State the blood parasite species.
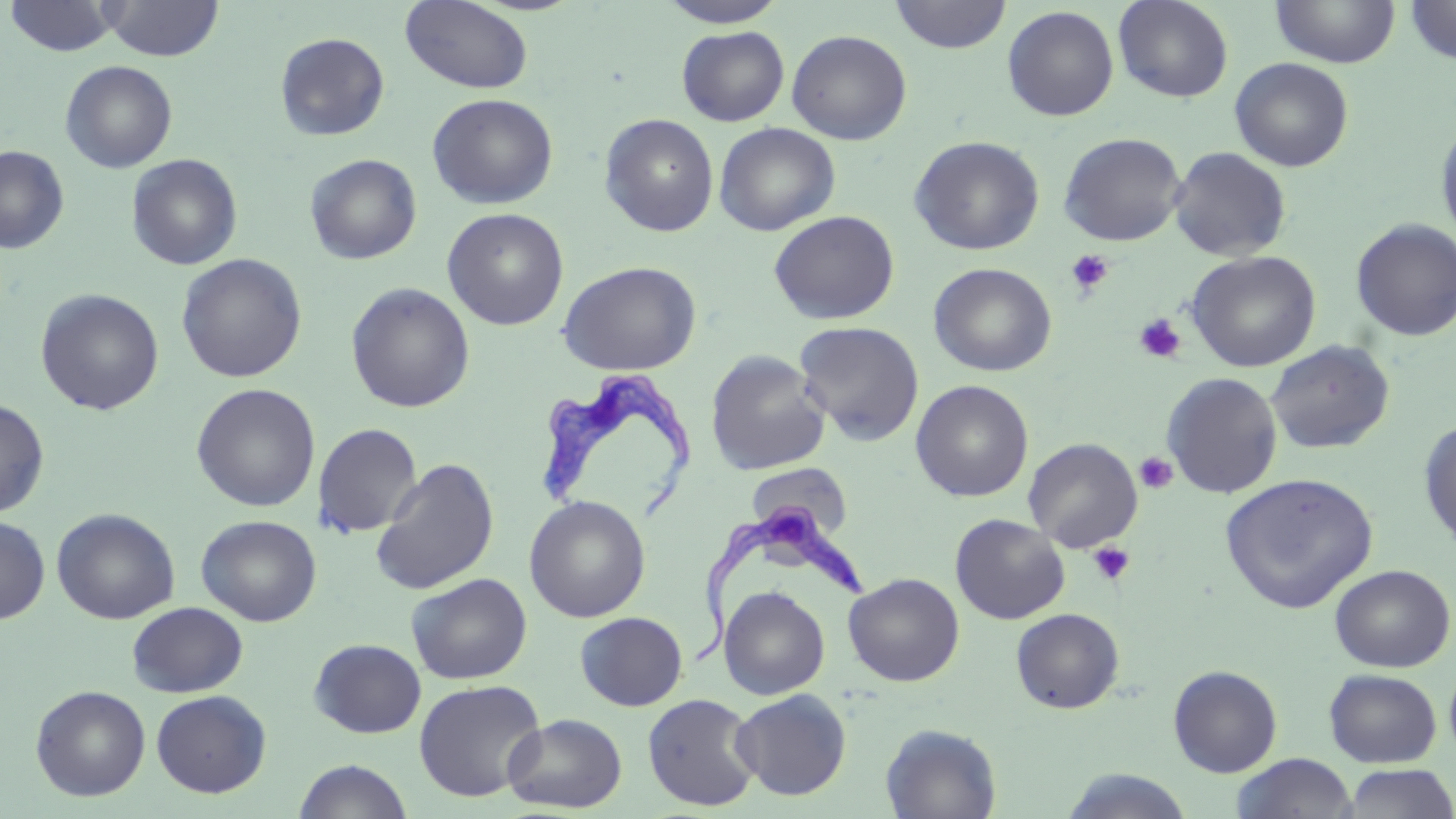
Trypanosoma brucei.

Summary:
  - Coordinate format: approximate bounding boxes as named x1/y1/x2/y2 corners in pixels
  - Platelet locations: (x1=1066, y1=249, x2=1114, y2=296), (x1=1134, y1=313, x2=1186, y2=363), (x1=1134, y1=451, x2=1178, y2=494), (x1=1088, y1=541, x2=1135, y2=586)
  - Trypanosoma brucei locations: (x1=532, y1=366, x2=698, y2=527), (x1=689, y1=499, x2=870, y2=666)
  - Uninfected red blood cell locations: (x1=4, y1=0, x2=120, y2=57), (x1=890, y1=0, x2=1012, y2=54), (x1=1113, y1=0, x2=1234, y2=103), (x1=1403, y1=0, x2=1456, y2=64), (x1=100, y1=1, x2=223, y2=61), (x1=400, y1=1, x2=534, y2=93), (x1=658, y1=1, x2=788, y2=28), (x1=1270, y1=1, x2=1400, y2=68), (x1=1002, y1=6, x2=1119, y2=121), (x1=677, y1=26, x2=789, y2=126), (x1=786, y1=29, x2=912, y2=145), (x1=275, y1=32, x2=390, y2=142), (x1=1230, y1=57, x2=1354, y2=172), (x1=60, y1=60, x2=177, y2=173), (x1=426, y1=92, x2=558, y2=209), (x1=599, y1=114, x2=719, y2=237), (x1=1435, y1=116, x2=1456, y2=248), (x1=714, y1=122, x2=840, y2=236), (x1=1058, y1=132, x2=1187, y2=246), (x1=909, y1=135, x2=1045, y2=255), (x1=0, y1=145, x2=69, y2=254), (x1=1168, y1=147, x2=1292, y2=262), (x1=127, y1=153, x2=242, y2=270), (x1=305, y1=154, x2=422, y2=265), (x1=442, y1=208, x2=569, y2=330), (x1=768, y1=210, x2=900, y2=325), (x1=1350, y1=218, x2=1456, y2=341), (x1=1185, y1=250, x2=1321, y2=372), (x1=176, y1=253, x2=306, y2=383), (x1=557, y1=260, x2=702, y2=376), (x1=929, y1=262, x2=1056, y2=376), (x1=345, y1=282, x2=475, y2=413), (x1=35, y1=288, x2=164, y2=415), (x1=793, y1=320, x2=925, y2=446), (x1=1265, y1=340, x2=1395, y2=454), (x1=704, y1=349, x2=830, y2=475), (x1=1161, y1=372, x2=1283, y2=499), (x1=910, y1=380, x2=1033, y2=502), (x1=190, y1=383, x2=320, y2=512), (x1=0, y1=400, x2=49, y2=517), (x1=1418, y1=417, x2=1456, y2=552), (x1=313, y1=422, x2=423, y2=538), (x1=1023, y1=438, x2=1143, y2=552), (x1=371, y1=457, x2=499, y2=595), (x1=745, y1=463, x2=853, y2=539), (x1=1219, y1=472, x2=1378, y2=614), (x1=524, y1=495, x2=651, y2=623), (x1=52, y1=508, x2=180, y2=624), (x1=196, y1=514, x2=321, y2=626), (x1=949, y1=514, x2=1070, y2=624), (x1=0, y1=516, x2=50, y2=624), (x1=1329, y1=564, x2=1455, y2=672), (x1=843, y1=572, x2=964, y2=686), (x1=406, y1=573, x2=533, y2=685), (x1=718, y1=583, x2=963, y2=696), (x1=719, y1=585, x2=830, y2=700), (x1=127, y1=601, x2=248, y2=698), (x1=1010, y1=608, x2=1124, y2=713), (x1=575, y1=611, x2=687, y2=711), (x1=309, y1=638, x2=426, y2=738), (x1=1444, y1=658, x2=1456, y2=764), (x1=1168, y1=665, x2=1282, y2=777), (x1=1323, y1=668, x2=1442, y2=768), (x1=413, y1=679, x2=547, y2=802), (x1=30, y1=685, x2=150, y2=801), (x1=731, y1=688, x2=852, y2=801), (x1=151, y1=690, x2=271, y2=798), (x1=642, y1=693, x2=761, y2=812), (x1=502, y1=713, x2=627, y2=813), (x1=880, y1=723, x2=1001, y2=819), (x1=1232, y1=753, x2=1358, y2=818), (x1=293, y1=759, x2=413, y2=819), (x1=1340, y1=764, x2=1456, y2=818), (x1=1059, y1=769, x2=1195, y2=818)
  - Field of view: one of a larger specimen
  - Modality: light microscopy
  - Magnification: 1000x
  - Image size: 1456×819 pixels
  - Stain: May-Grünwald-Giemsa
  - Preparation: thin blood film